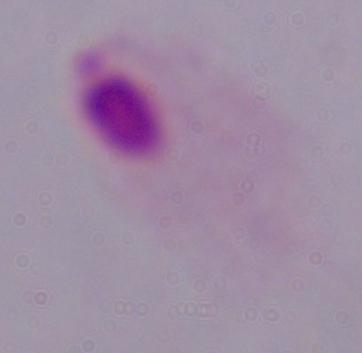

modality = micrograph
magnification = 1000x
identification = trichomonad